Identify the parasite.
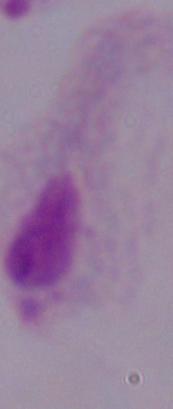

This is a trichomonad.

Summary:
  - Magnification: 1000x
  - Modality: micrograph